Comment on the morphology of the red blood cells.
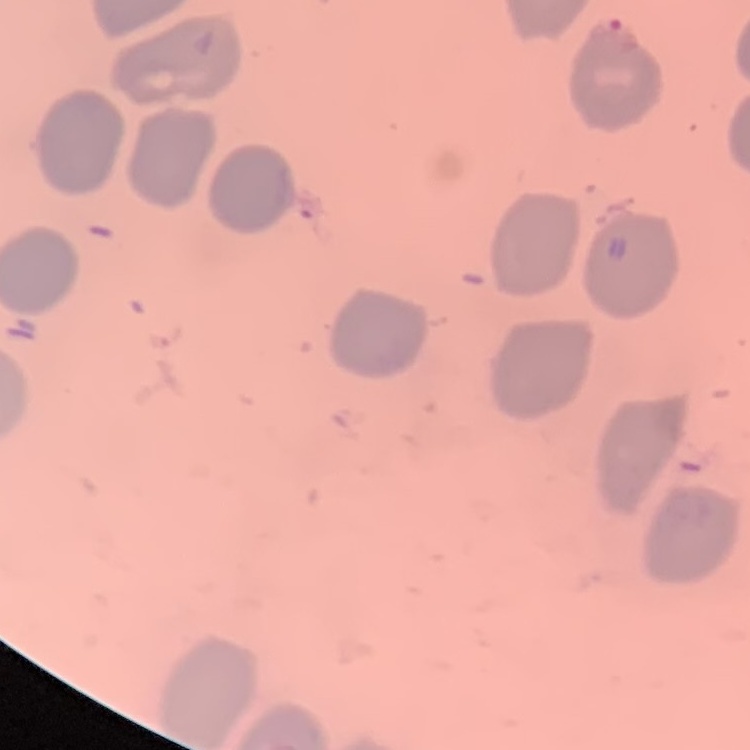

They show no rouleaux formation.

Stained with either Field's or Giemsa. Thin blood film. One tile cut from a larger photomicrograph.